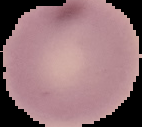
Summary:
  - Preparation: thin blood smear
  - Malaria status: uninfected
  - Image type: cell region segmented out of the field of view; surrounding area masked to black
  - Image size: 142×127 pixels